Outline each white blood cell.
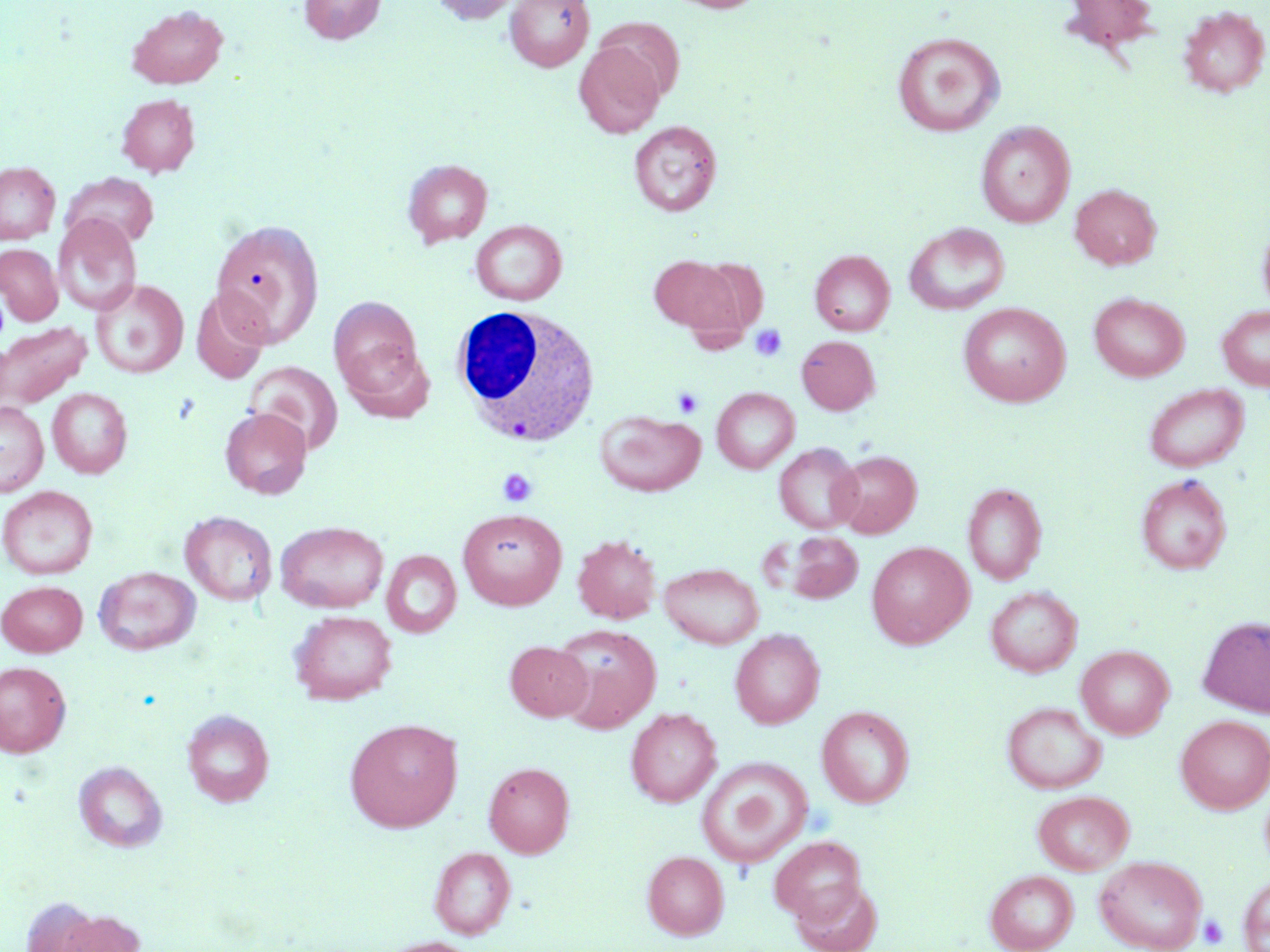
Approximate bounding boxes as (x1, y1, x2, y2) in pixels.
White blood cells: (450, 304, 601, 448).

slide-level diagnosis = no evidence of blood parasites
stain = May-Grünwald-Giemsa
modality = optical microscopy
field of view = single
platelet locations = approximate bounding boxes as (x1, y1, x2, y2) in pixels: (749, 324, 787, 362), (673, 387, 704, 419), (497, 468, 538, 507), (1199, 915, 1229, 949)
magnification = 1000x
image size = 1270×952 pixels
preparation = thin blood film
uninfected red blood cell locations = approximate bounding boxes as (x1, y1, x2, y2) in pixels: (298, 0, 386, 45), (430, 0, 519, 24), (665, 0, 766, 13), (1060, 0, 1161, 56), (504, 1, 594, 72), (127, 5, 228, 88), (1179, 5, 1269, 97), (594, 17, 686, 100), (893, 32, 1004, 136), (574, 42, 665, 138), (116, 93, 200, 177), (629, 120, 722, 216), (976, 121, 1076, 228), (403, 159, 493, 248), (0, 162, 60, 244), (61, 173, 160, 250), (1070, 184, 1161, 270), (53, 214, 141, 316), (213, 218, 325, 346), (1257, 218, 1270, 317), (471, 220, 567, 305), (905, 223, 1010, 315), (0, 244, 63, 325), (810, 250, 895, 335), (649, 255, 745, 336), (90, 279, 188, 378), (192, 288, 271, 384), (1089, 292, 1188, 381), (329, 296, 423, 394), (958, 302, 1070, 406), (1217, 305, 1270, 390), (0, 322, 92, 408), (797, 336, 879, 415), (340, 343, 436, 424), (245, 361, 344, 454), (1144, 384, 1247, 472), (47, 388, 132, 478), (711, 388, 799, 473), (0, 401, 48, 497), (220, 408, 312, 499), (595, 410, 705, 496), (774, 443, 864, 533), (831, 450, 922, 538), (1136, 474, 1232, 574), (962, 482, 1047, 585), (0, 485, 98, 579), (457, 507, 567, 610), (180, 511, 278, 606), (275, 520, 388, 613), (785, 532, 863, 603), (573, 534, 662, 623), (866, 542, 973, 648), (382, 550, 461, 638), (659, 562, 764, 649), (94, 566, 201, 655), (1, 580, 87, 656), (985, 586, 1081, 677), (289, 609, 397, 705), (1198, 616, 1270, 717), (552, 624, 661, 733), (730, 628, 825, 729), (504, 641, 593, 721), (1076, 645, 1174, 739), (0, 661, 71, 757), (1001, 701, 1106, 794), (817, 705, 915, 808), (626, 708, 721, 807), (182, 709, 274, 807), (1176, 715, 1270, 814), (344, 718, 463, 832), (696, 757, 813, 868), (74, 760, 167, 851), (483, 761, 574, 858), (1033, 790, 1134, 874), (769, 835, 867, 923), (429, 846, 516, 939), (642, 850, 729, 939), (1094, 855, 1207, 952), (985, 869, 1078, 952), (1238, 874, 1270, 952), (791, 878, 883, 952), (48, 908, 146, 952), (375, 937, 482, 952)